Classify this cell by malaria status.
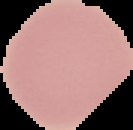

It is uninfected.

Summary:
  - Preparation: thin blood smear
  - Image type: cell region segmented out of the field of view; surrounding area masked to black
  - Image size: 133×130 pixels